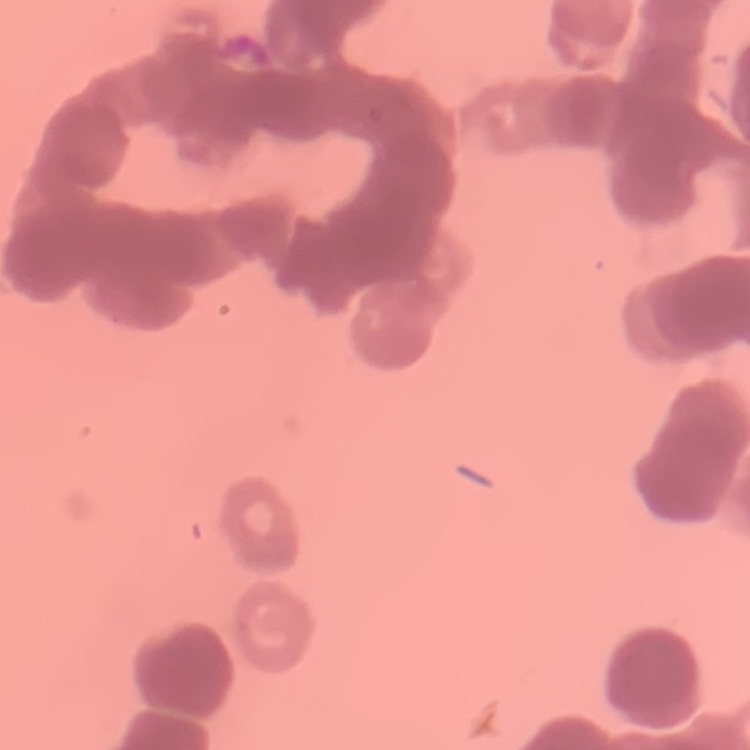
red_blood_cell_morphology: rouleaux formation
image_type: one tile cut from a larger photomicrograph
stain: Field's or Giemsa
preparation: thin blood film